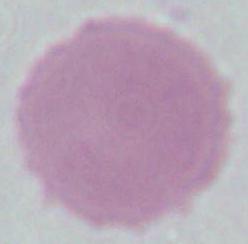
Summary:
  - Modality: photomicrograph
  - Magnification: 1000x
  - Identification: red blood cell